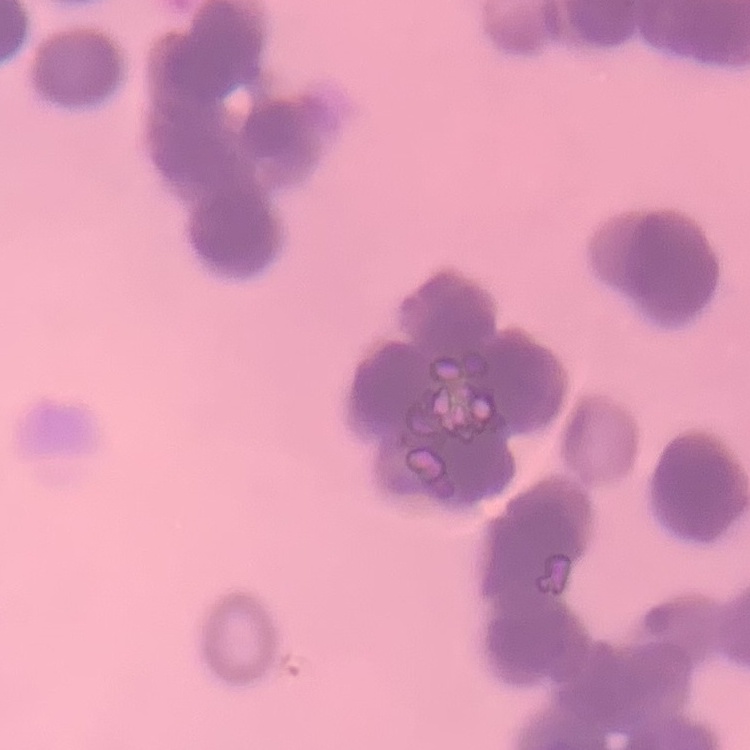 The erythrocytes exhibit rouleaux formation. One tile cut from a larger photomicrograph. Thin blood film. Stained with either Field's or Giemsa.